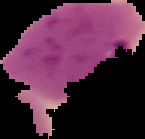
{
  "preparation": "thin blood smear",
  "result": "malaria parasites identified",
  "image_size": "145×139 pixels",
  "image_type": "cell region segmented out of the field of view; surrounding area masked to black"
}